Assess the morphology of the erythrocytes.
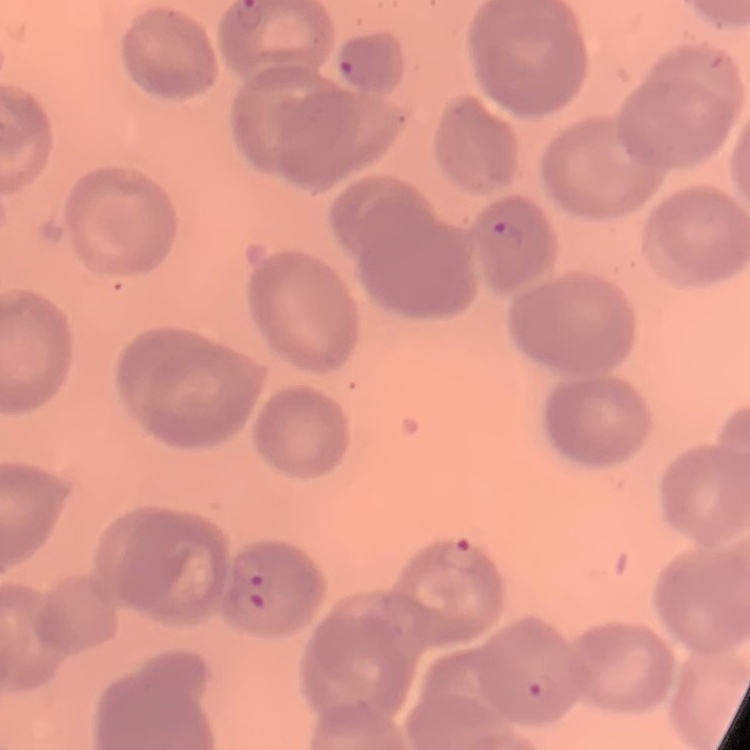

They show no rouleaux formation.

Summary:
  - Stain: Field's or Giemsa
  - Preparation: thin peripheral smear
  - Image type: one tile cut from a larger photomicrograph